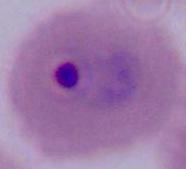 Micrograph. A Plasmodium parasite is seen. Captured at either 400x or 1000x magnification.